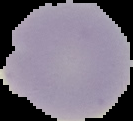 Result: no Plasmodium parasites detected. Cell region segmented out of the field of view; the surrounding area is masked to black. From a thin blood smear. Image is 133×121 pixels.